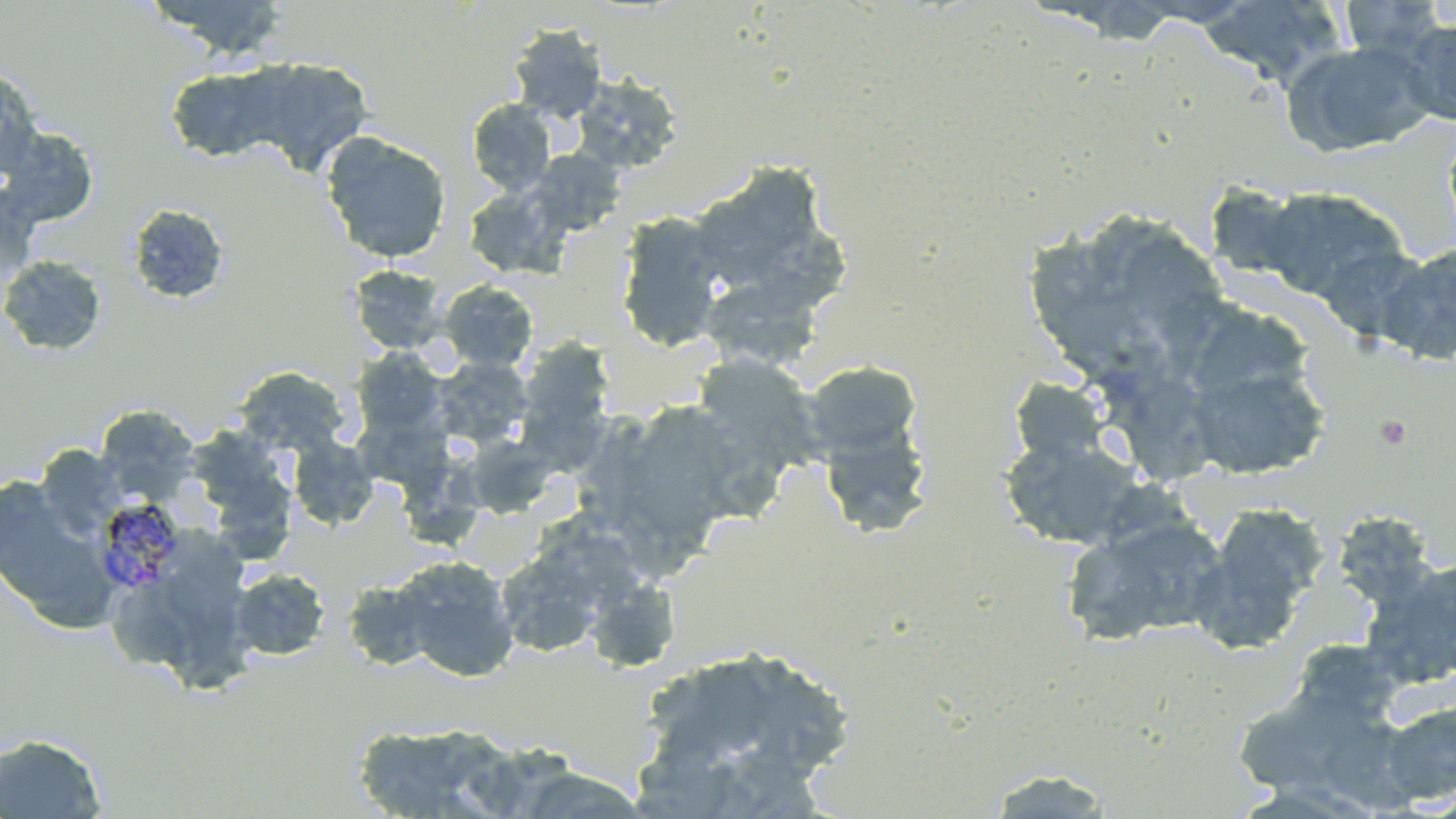 Approximate bounding boxes as (x1, y1, x2, y2) in pixels. Uninfected red blood cell locations: (145, 0, 290, 60), (1338, 0, 1449, 62), (1198, 1, 1347, 85), (1398, 17, 1456, 126), (508, 23, 608, 123), (1280, 39, 1437, 158), (233, 56, 374, 177), (0, 64, 42, 181), (164, 64, 290, 164), (570, 74, 683, 174), (466, 99, 557, 197), (0, 125, 101, 229), (320, 131, 451, 264), (526, 148, 626, 238), (725, 163, 837, 270), (1203, 183, 1314, 284), (463, 185, 569, 279), (1255, 186, 1409, 305), (128, 203, 229, 305), (615, 211, 727, 352), (1123, 224, 1232, 340), (744, 229, 854, 296), (1026, 234, 1113, 305), (1377, 243, 1456, 366), (0, 255, 108, 356), (348, 264, 448, 355), (715, 275, 838, 352), (438, 280, 538, 373), (1046, 286, 1168, 389), (1200, 310, 1321, 387), (535, 332, 611, 420), (351, 348, 447, 440), (690, 351, 823, 482), (433, 357, 533, 450), (1183, 358, 1330, 480), (801, 360, 923, 464), (233, 367, 351, 457), (1127, 372, 1228, 475), (1010, 376, 1110, 465), (96, 406, 200, 501), (653, 409, 737, 525), (185, 422, 284, 510), (471, 434, 559, 514), (999, 434, 1148, 550), (287, 435, 380, 531), (34, 444, 126, 538), (401, 450, 481, 557), (0, 472, 117, 630), (227, 472, 299, 561), (1191, 502, 1330, 650), (1330, 511, 1438, 611), (1061, 512, 1229, 648), (174, 534, 252, 620), (493, 537, 620, 659), (390, 555, 520, 681), (1363, 555, 1456, 689), (230, 568, 330, 661), (341, 576, 439, 672), (111, 586, 186, 672), (594, 586, 682, 674), (170, 604, 252, 695), (1288, 638, 1408, 729), (636, 642, 858, 804), (1231, 682, 1399, 804), (1379, 698, 1456, 806), (348, 722, 513, 818), (0, 733, 108, 818), (520, 750, 656, 819), (981, 767, 1119, 817). Plasmodium malariae-infected red blood cell locations: (93, 497, 187, 594). Platelet locations: (1373, 414, 1413, 451). Slide-level diagnosis: Plasmodium malariae. Thin blood smear. Image is 1456×819 pixels. Captured at 1000x magnification. May-Grünwald-Giemsa-stained preparation. Optical microscopy. One field of a larger specimen.